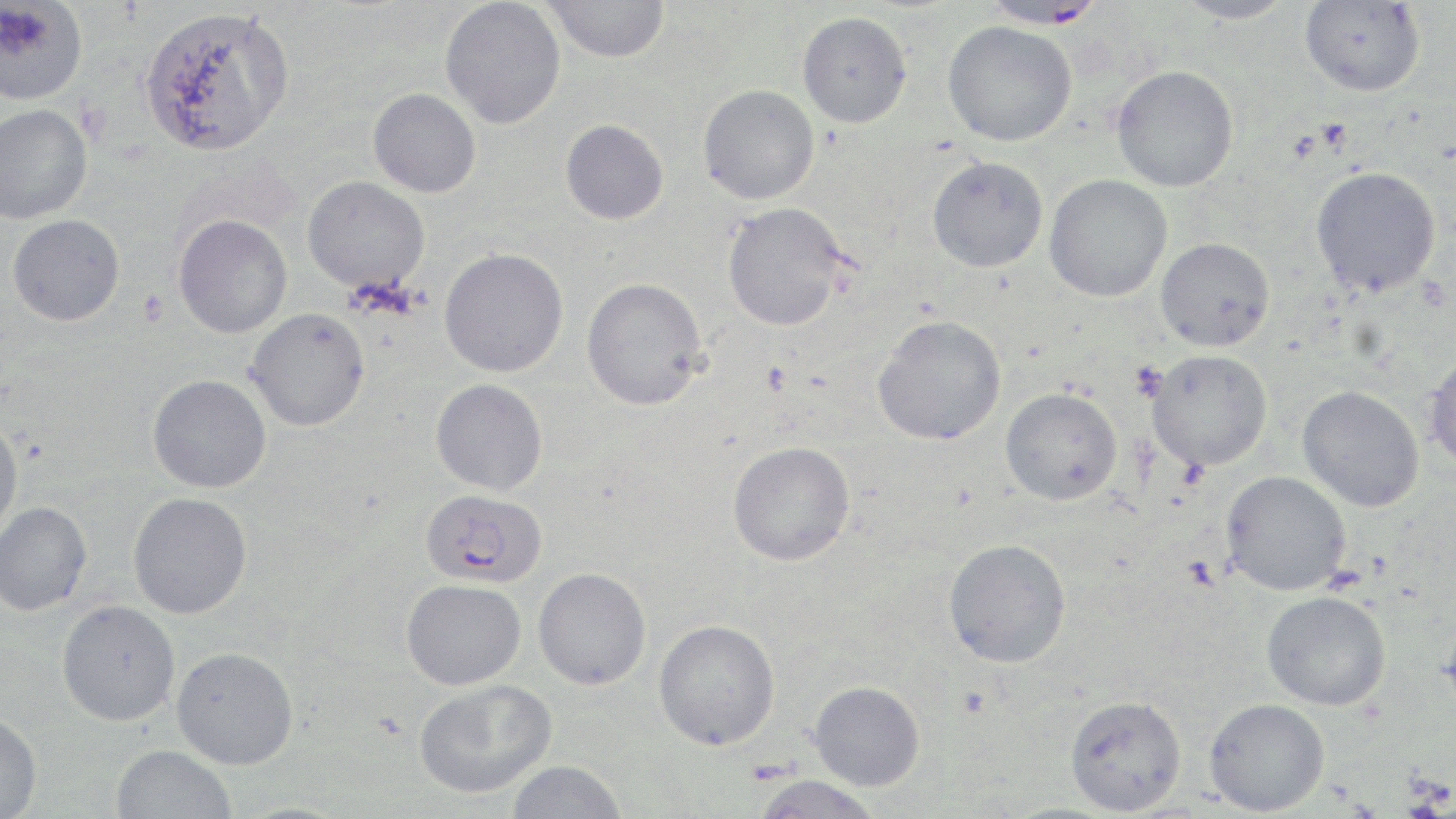
Approximate bounding boxes as (x1,y1)-(x2,y2) corner pairs in pixels. Uninfected red blood cell locations: (542,0)-(671,63), (1174,0)-(1295,25), (1299,0)-(1425,97), (0,1)-(88,105), (440,1)-(565,129), (139,5)-(295,157), (797,11)-(912,128), (942,21)-(1077,146), (1111,65)-(1239,192), (697,84)-(819,204), (368,88)-(481,197), (0,104)-(92,224), (560,119)-(669,224), (927,155)-(1048,272), (1310,166)-(1442,297), (1044,174)-(1172,302), (302,176)-(430,294), (721,202)-(852,332), (7,214)-(125,326), (173,214)-(292,338), (1155,237)-(1275,351), (439,248)-(569,377), (581,277)-(708,410), (245,307)-(370,431), (872,315)-(1006,446), (1146,349)-(1272,471), (1425,350)-(1456,472), (147,374)-(271,493), (430,378)-(547,495), (1297,386)-(1424,512), (1000,387)-(1122,505), (0,417)-(23,542), (727,441)-(855,566), (1221,470)-(1351,596), (128,492)-(252,619), (0,501)-(92,615), (943,538)-(1071,667), (533,567)-(651,690), (401,579)-(526,689), (1262,591)-(1391,710), (56,600)-(180,726), (1439,606)-(1456,720), (653,619)-(781,750), (171,646)-(298,768), (414,678)-(557,798), (808,681)-(925,790), (1065,694)-(1187,815), (1204,697)-(1329,816), (0,713)-(42,819), (111,745)-(237,819), (505,760)-(627,819), (749,775)-(885,819), (228,800)-(356,818). Plasmodium falciparum-infected red blood cell locations: (979,1)-(1107,29), (420,487)-(547,588). Platelet locations: (138,290)-(169,325), (1130,361)-(1168,401). Slide-level diagnosis: Plasmodium falciparum. Thin blood smear. May-Grünwald-Giemsa stain. Captured at 1000x magnification. Light microscopy. Single field of view. Image is 1456×819 pixels.